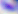 Captured at 400x magnification. Photomicrograph. Toxoplasma gondii is seen.